Identify the parasite.
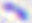

Toxoplasma gondii.

Summary:
  - Modality: photomicrograph
  - Magnification: 400x